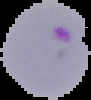
Summary:
  - Image size: 91×100 pixels
  - Malaria status: parasitized
  - Preparation: thin blood smear
  - Image type: segmented cell region on a black background